Report the malaria status of this cell.
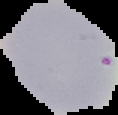
It is uninfected.

Summary:
  - Preparation: thin blood smear
  - Image size: 118×115 pixels
  - Image type: cell region segmented out of the field of view; surrounding area masked to black